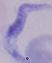

magnification: 1000x
identification: trypanosome
modality: micrograph